Report the malaria status of this cell.
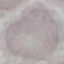
It is uninfected.

Acquired by smartphone through the microscope eyepiece. Giemsa-stained preparation. Thin smear of blood. Cell patch, automatically extracted from a larger field of view and resized to 64 × 64 pixels.